Evaluate for Plasmodium parasites.
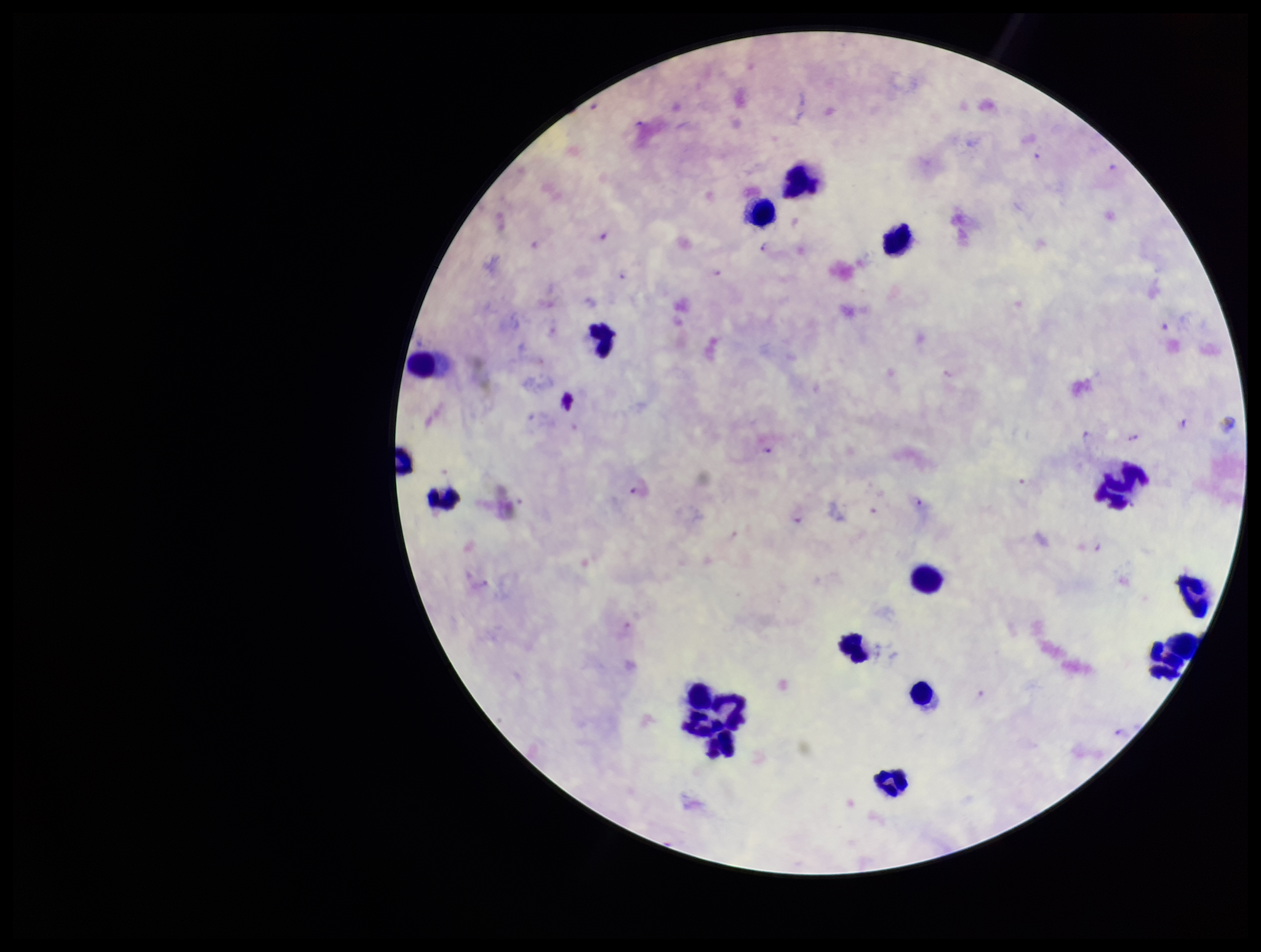
Detected.

Giemsa stain. Parasite count: 12. Preparation: thick smear. Species reported for this patient: Plasmodium falciparum. Leukocyte count: 15. Smartphone photograph taken through the eyepiece of a microscope. Image is 1261×952 pixels. Single field of view. Patient malaria status: positive.